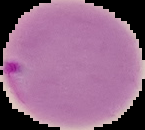 Image is 145×130 pixels. From a thin blood smear. The area outside the segmented cell region is set to black. Result: Plasmodium parasites identified.